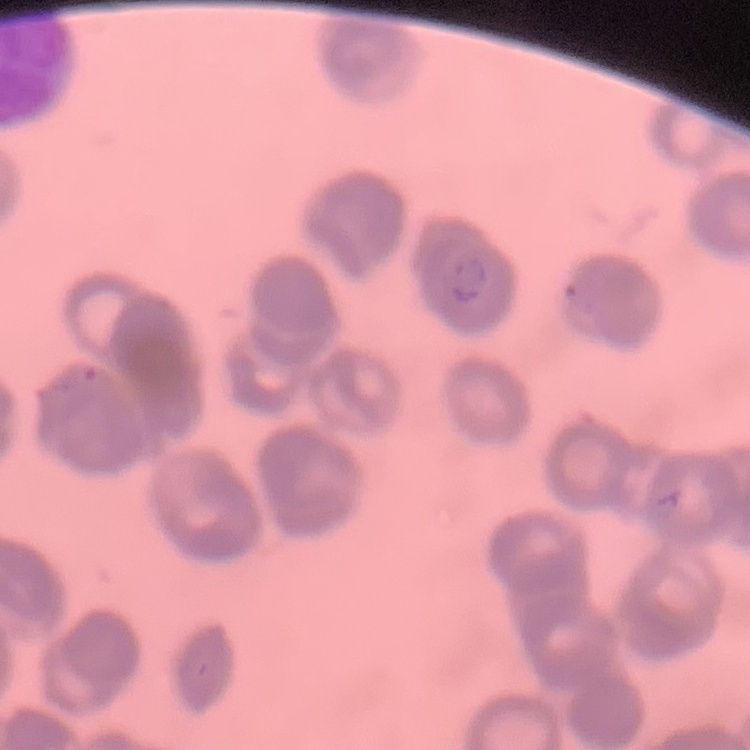

The red blood cells show rouleaux formation. Thin peripheral smear. Square crop of a larger photomicrograph. Stained with either Field's or Giemsa.